Classify this cell by malaria status.
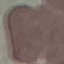
Uninfected.

Thin blood film. Giemsa-stained preparation. Cell patch, automatically extracted from a larger field of view and resized to 64 × 64 pixels. Photographed with a smartphone camera at the microscope eyepiece.